Report the malaria status of this cell.
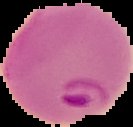

It is parasitized.

image_size: 133×127 pixels
image_type: cell region segmented out of the field of view; surrounding area masked to black
preparation: thin blood smear